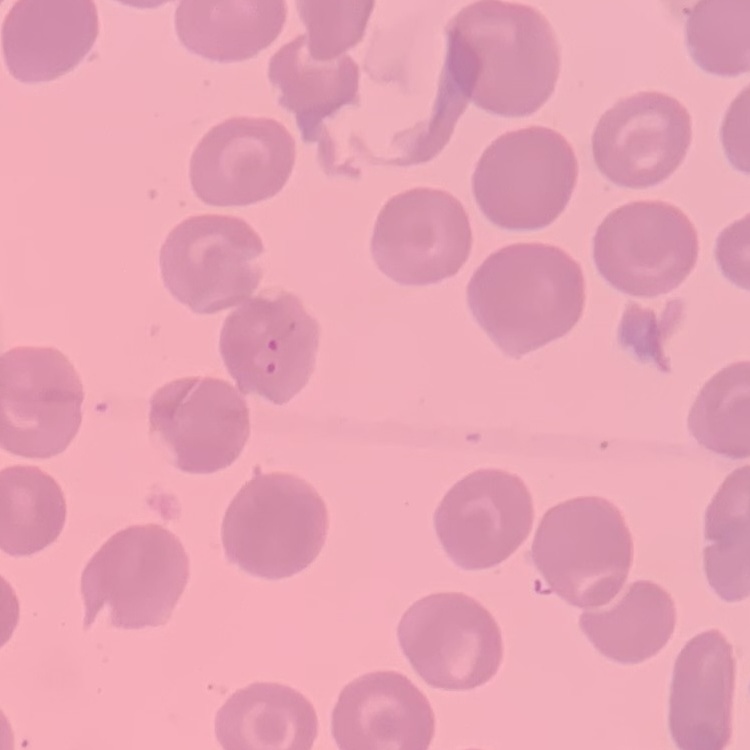
Summary:
  - Red blood cell morphology: no rouleaux formation
  - Image type: square crop of a larger photomicrograph
  - Preparation: thin blood smear
  - Stain: Field's or Giemsa